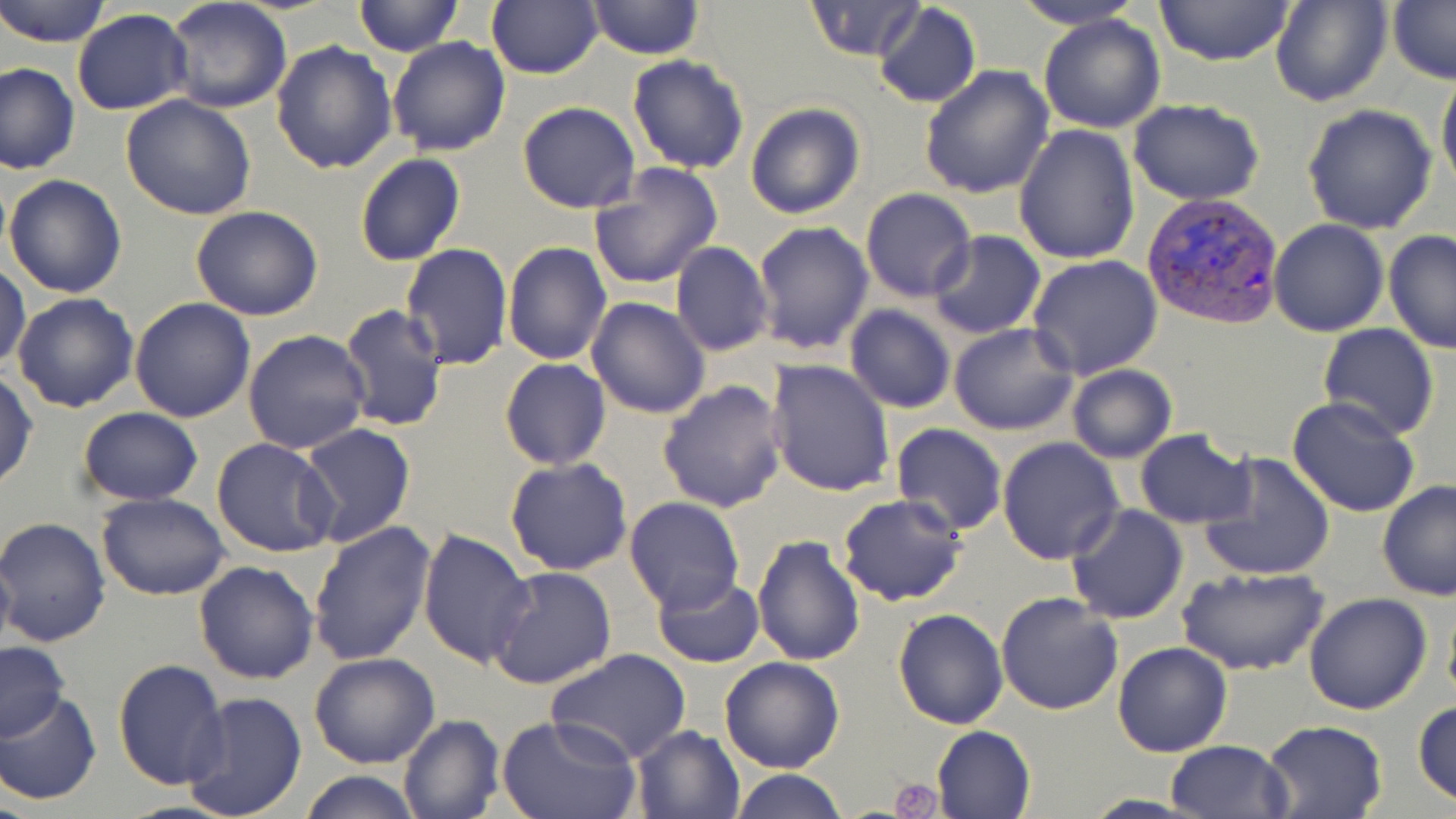
slide-level diagnosis = Plasmodium vivax
magnification = 1000x
platelet locations = approximate bounding boxes as [x1, y1, x2, y2] in pixels: [889, 777, 940, 818]
modality = light microscopy
Plasmodium vivax-infected red blood cell locations = approximate bounding boxes as [x1, y1, x2, y2] in pixels: [1141, 190, 1285, 329]
preparation = thin blood smear
stain = May-Grünwald-Giemsa
uninfected red blood cell locations = approximate bounding boxes as [x1, y1, x2, y2] in pixels: [0, 0, 112, 47], [164, 0, 292, 114], [352, 0, 463, 57], [586, 0, 704, 60], [804, 0, 927, 62], [1007, 0, 1149, 28], [1152, 0, 1297, 68], [1270, 0, 1392, 107], [1387, 0, 1456, 85], [486, 1, 603, 79], [873, 3, 981, 109], [72, 10, 193, 113], [1038, 14, 1165, 134], [386, 35, 510, 157], [271, 40, 398, 175], [626, 53, 750, 173], [1, 61, 79, 176], [920, 65, 1055, 200], [1437, 69, 1456, 196], [120, 95, 257, 221], [1128, 98, 1266, 204], [517, 101, 640, 214], [745, 101, 867, 220], [1302, 103, 1438, 234], [1014, 124, 1140, 265], [354, 154, 465, 267], [588, 164, 723, 289], [3, 174, 129, 298], [860, 188, 976, 301], [190, 204, 324, 321], [1267, 219, 1390, 336], [752, 220, 875, 357], [929, 230, 1046, 339], [1384, 230, 1456, 353], [670, 241, 773, 357], [501, 242, 613, 365], [400, 244, 513, 371], [1026, 254, 1163, 379], [1, 260, 29, 373], [12, 292, 139, 413], [586, 297, 711, 420], [130, 299, 255, 422], [338, 303, 448, 432], [844, 305, 958, 414], [949, 322, 1079, 435], [1317, 324, 1438, 441], [243, 329, 371, 455], [501, 358, 611, 471], [766, 359, 896, 498], [1067, 364, 1177, 462], [0, 371, 38, 491], [657, 378, 787, 514], [1287, 397, 1422, 517], [76, 407, 203, 506], [298, 423, 416, 548], [890, 423, 1008, 536], [1134, 430, 1254, 527], [212, 436, 342, 559], [997, 438, 1124, 565], [1199, 451, 1335, 581], [504, 456, 633, 574], [1378, 481, 1456, 601], [97, 492, 231, 601], [837, 493, 967, 606], [623, 496, 745, 615], [1065, 505, 1188, 623], [1, 518, 114, 648], [309, 522, 437, 667], [418, 526, 535, 669], [751, 534, 865, 666], [0, 547, 16, 664], [193, 560, 321, 684], [489, 564, 619, 689], [1176, 565, 1330, 677], [650, 573, 765, 667], [996, 590, 1125, 714], [1305, 592, 1432, 714], [1442, 594, 1456, 713], [893, 607, 1009, 729], [0, 640, 72, 741], [1112, 640, 1233, 757], [546, 649, 694, 766], [309, 653, 440, 768], [719, 656, 846, 773], [112, 660, 229, 790], [0, 691, 101, 805], [182, 691, 308, 819], [1412, 698, 1456, 809], [397, 714, 504, 819], [498, 715, 643, 819], [1260, 718, 1388, 819], [629, 724, 746, 818], [932, 725, 1036, 817], [1166, 739, 1293, 819], [728, 768, 849, 819], [302, 769, 421, 819]
image size = 1456×819 pixels
field of view = one of a larger specimen